Identify the blood parasite species.
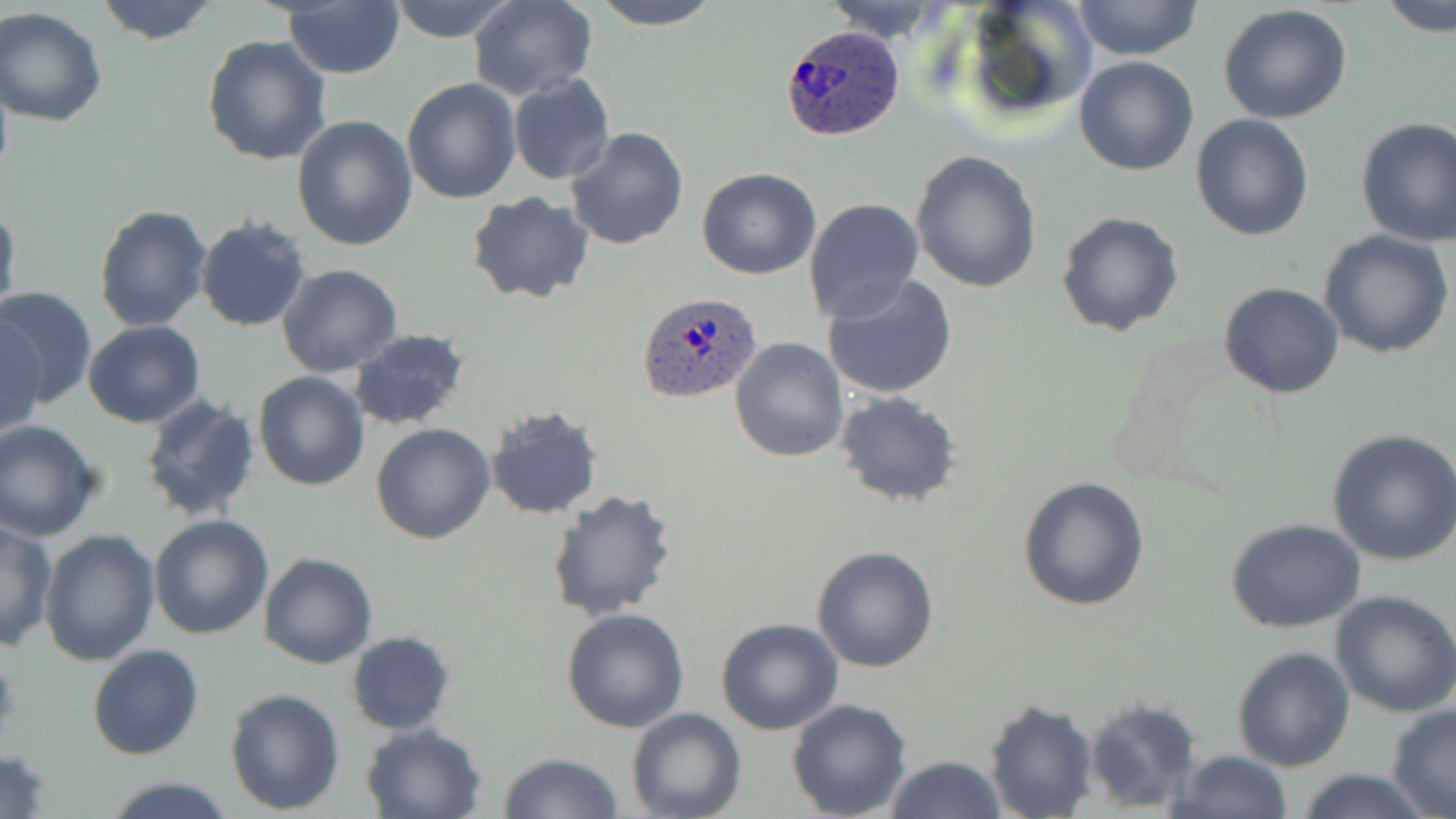

Plasmodium ovale.

Summary:
  - Coordinate format: approximate bounding boxes as (x1,y1)-(x2,y2) corner pairs in pixels
  - Plasmodium ovale-infected red blood cell locations: (780,25)-(907,142), (635,291)-(762,403)
  - Uninfected red blood cell locations: (94,0)-(219,45), (386,0)-(520,43), (468,0)-(599,100), (590,0)-(723,29), (958,0)-(1097,126), (1072,0)-(1204,63), (818,1)-(952,43), (1378,1)-(1456,38), (283,3)-(405,79), (1219,5)-(1353,125), (0,7)-(108,127), (202,35)-(331,165), (1074,56)-(1199,176), (507,75)-(615,187), (401,79)-(522,204), (291,114)-(418,251), (1191,114)-(1313,242), (1354,116)-(1456,245), (566,127)-(690,249), (910,151)-(1042,292), (696,168)-(821,279), (806,181)-(1026,313), (467,193)-(596,305), (803,197)-(923,323), (0,198)-(21,327), (94,205)-(213,332), (1055,211)-(1184,337), (195,217)-(311,333), (1319,230)-(1454,358), (277,264)-(402,378), (823,273)-(958,399), (1219,283)-(1345,400), (0,285)-(98,409), (2,317)-(45,442), (82,321)-(205,429), (348,327)-(472,432), (729,336)-(849,463), (253,372)-(371,491), (834,390)-(963,510), (139,395)-(262,522), (485,406)-(603,520), (0,421)-(102,541), (370,423)-(495,545), (1327,427)-(1456,565), (1017,475)-(1151,612), (543,489)-(677,622), (149,516)-(274,639), (1225,518)-(1368,633), (1,519)-(57,650), (40,529)-(160,666), (810,545)-(940,673), (259,552)-(378,669), (1330,591)-(1456,716), (562,608)-(690,733), (716,618)-(844,735), (346,630)-(454,735), (88,645)-(204,760), (1232,645)-(1357,771), (225,688)-(345,812), (1083,697)-(1202,813), (982,698)-(1100,819), (788,699)-(913,819), (1385,703)-(1456,818), (626,707)-(746,819), (361,722)-(486,819), (0,748)-(53,818), (1170,749)-(1293,819), (499,752)-(622,819), (885,755)-(1007,819), (1294,766)-(1436,819), (105,777)-(235,817)
  - Modality: light microscopy
  - Image size: 1456×819 pixels
  - Field of view: one of a larger specimen
  - Magnification: 1000x
  - Preparation: thin blood film
  - Stain: May-Grünwald-Giemsa